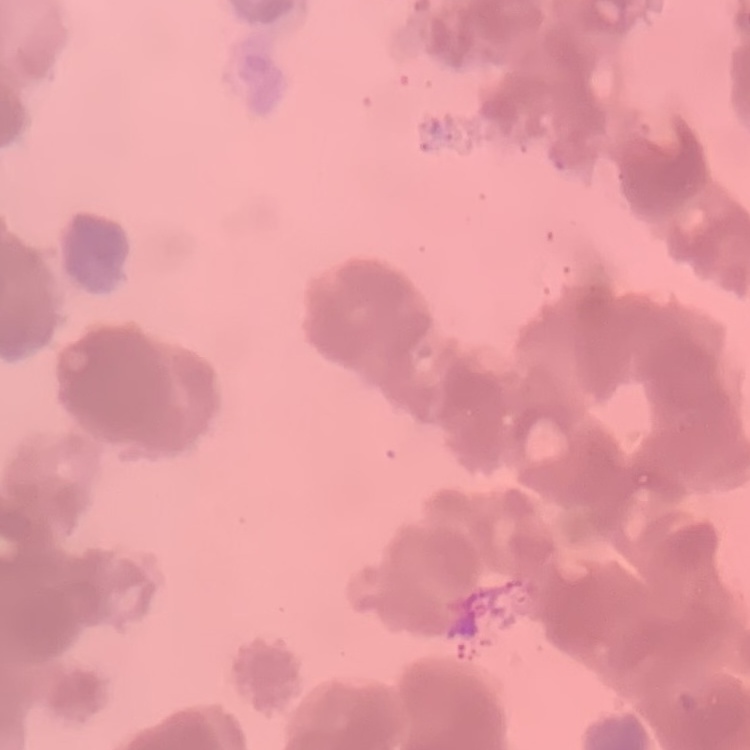
The red blood cells show rouleaux formation. Thin blood smear. Stained with either Field's or Giemsa. Square crop of a larger photomicrograph.